State which cell type is depicted.
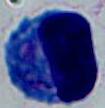
A leukocyte.

magnification: 1000x
modality: micrograph